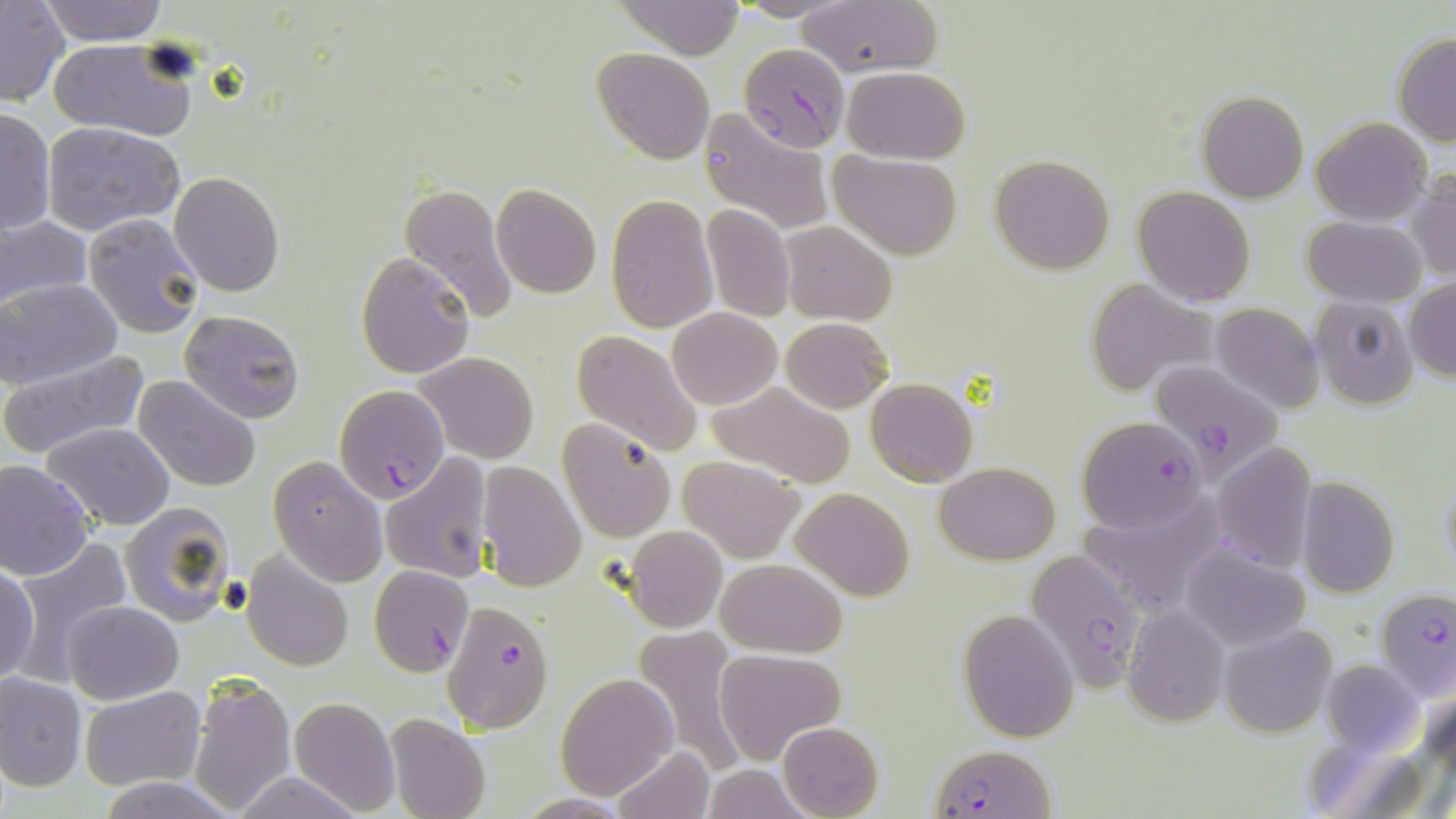
slide_level_diagnosis: Plasmodium falciparum
image_size: 1456×819 pixels
uninfected_red_blood_cell_locations: 'approximate bounding boxes as [x1, y1, x2, y2] in pixels: [1, 0, 69, 106], [38, 0, 170, 45], [731, 0, 849, 22], [797, 0, 942, 77], [614, 1, 746, 58], [1393, 33, 1456, 144], [49, 39, 195, 141], [591, 47, 712, 164], [841, 66, 970, 163], [1196, 92, 1308, 203], [0, 106, 55, 238], [698, 108, 834, 235], [1311, 117, 1432, 225], [41, 120, 184, 236], [830, 150, 963, 259], [990, 155, 1113, 274], [1405, 170, 1456, 282], [170, 172, 284, 296], [399, 182, 517, 328], [492, 183, 601, 298], [1132, 186, 1256, 307], [607, 194, 719, 331], [702, 204, 794, 322], [83, 214, 204, 338], [0, 215, 91, 314], [1304, 216, 1425, 306], [781, 221, 896, 326], [355, 253, 473, 379], [1405, 277, 1456, 383], [0, 278, 121, 387], [1085, 279, 1213, 395], [1310, 298, 1418, 410], [1210, 303, 1322, 413], [667, 308, 781, 410], [178, 309, 304, 423], [781, 316, 893, 414], [572, 329, 705, 458], [1, 347, 147, 459], [416, 351, 540, 463], [134, 375, 260, 492], [864, 376, 978, 487], [710, 382, 855, 488], [555, 418, 677, 543], [43, 422, 174, 531], [1211, 442, 1317, 574], [379, 453, 492, 585], [679, 455, 804, 561], [267, 458, 387, 587], [0, 459, 95, 579], [935, 461, 1059, 564], [476, 462, 587, 592], [1439, 467, 1455, 576], [1295, 476, 1400, 597], [791, 487, 913, 602], [119, 504, 235, 626], [623, 525, 727, 632], [10, 537, 134, 678], [1180, 545, 1310, 652], [242, 552, 353, 670], [718, 559, 847, 658], [1, 560, 40, 686], [61, 600, 182, 704], [1121, 601, 1230, 730], [958, 608, 1079, 742], [1219, 624, 1336, 738], [632, 625, 749, 777], [714, 647, 846, 766], [1316, 659, 1427, 763], [0, 672, 85, 791], [556, 674, 677, 798], [189, 676, 295, 812], [79, 688, 203, 789], [288, 697, 401, 816], [386, 715, 490, 819], [778, 722, 884, 819], [612, 744, 716, 819], [698, 766, 808, 818], [235, 772, 362, 819], [98, 775, 234, 818], [516, 795, 635, 818]'
magnification: 1000x
modality: optical microscopy
stain: May-Grünwald-Giemsa
plasmodium_falciparum_infected_red_blood_cell_locations: 'approximate bounding boxes as [x1, y1, x2, y2] in pixels: [741, 49, 857, 153], [1155, 359, 1289, 487], [334, 384, 450, 502], [1078, 417, 1205, 532], [1025, 548, 1146, 693], [369, 565, 474, 678], [1376, 587, 1456, 703], [443, 600, 554, 733], [932, 746, 1054, 817]'
preparation: thin blood film
field_of_view: one of a larger specimen